Point out each Plasmodium parasite.
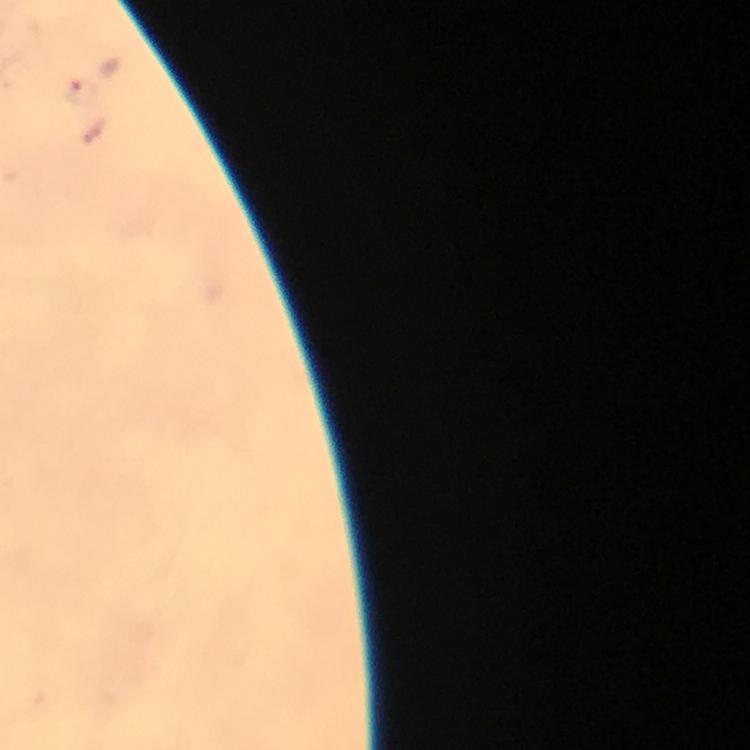
Approximate object centers, in pixels from the top-left corner.
Plasmodium parasites: (x=83, y=91).

Image is 750×750 pixels. Immersion oil was used. At 100x magnification. Cropped region of a single field of view. Giemsa stain. Photographed through the microscope with a smartphone camera. From a diagnostic examination for malaria. Thick blood smear.